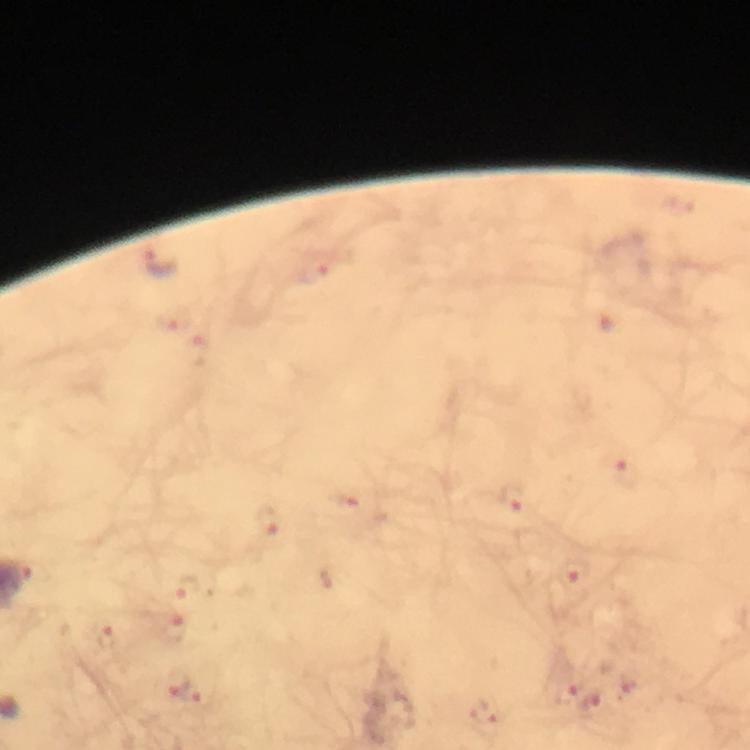
Approximate centers as (x, y) in pixels. Plasmodium parasite locations: (161, 263), (314, 271), (172, 319), (201, 351), (627, 473), (511, 498), (269, 520), (578, 575), (183, 586), (106, 636), (178, 682), (564, 690), (202, 698), (594, 703), (488, 712). Image is 750×750 pixels. Photographed through the microscope with a smartphone camera. From a malaria diagnostic workup. Giemsa stain. Thick blood smear. Cropped region of a single field of view. At 100x magnification. Immersion oil applied.